Report the malaria status.
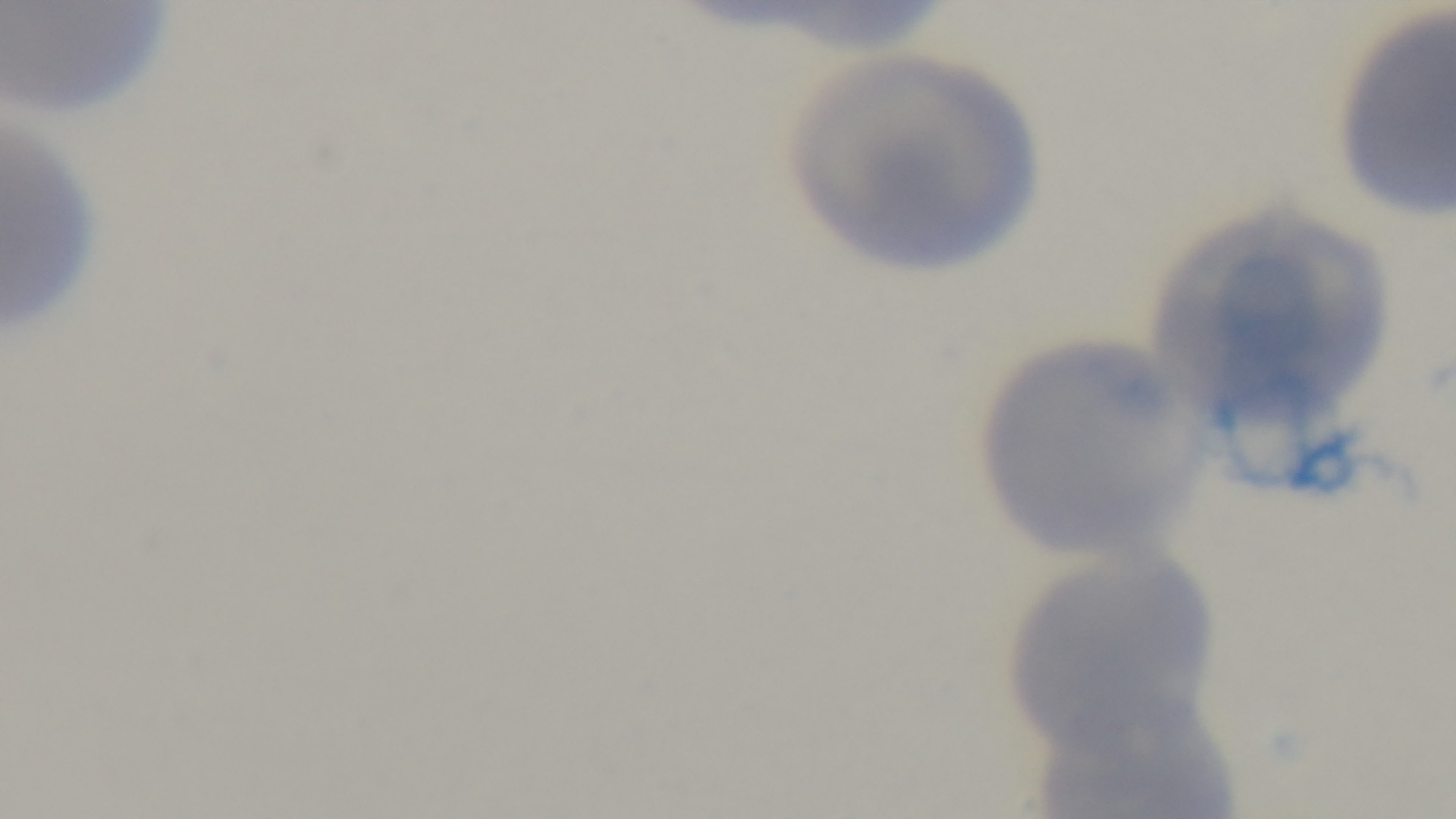
Negative.

modality = light microscopy
capture = mounted 4K digital camera
stain = Giemsa
objective = 100x oil immersion
field of view = one from the slide
preparation = thin smear